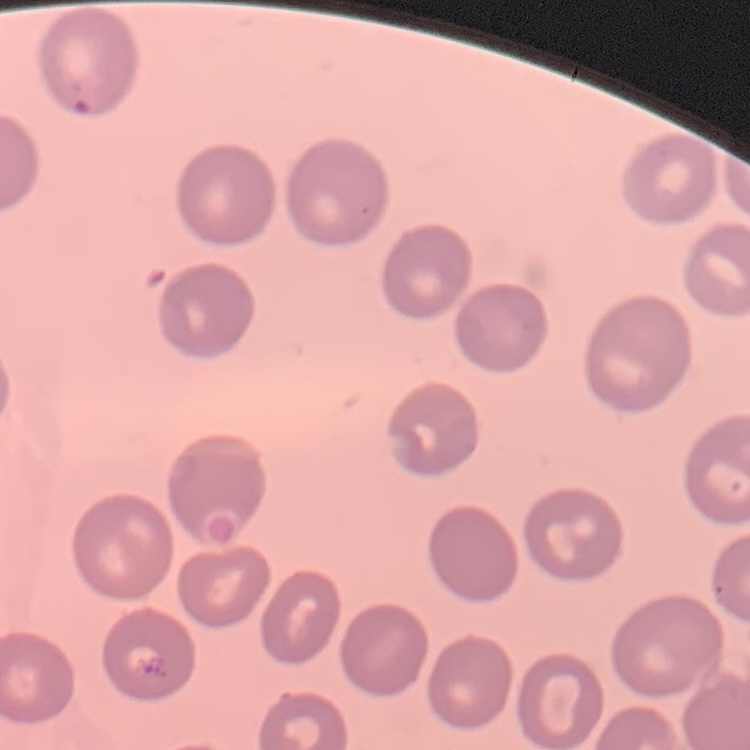
The erythrocytes show no rouleaux formation. Stained with either Field's or Giemsa. Thin peripheral smear. One tile cut from a larger photomicrograph.